Classify this cell by malaria status.
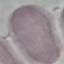

Uninfected.

Summary:
  - Preparation: thin blood film
  - Stain: Giemsa
  - Image type: cell patch, automatically extracted from a larger field of view and resized to 64 × 64 pixels
  - Capture: smartphone through the microscope eyepiece